Assess this cell for malaria.
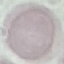
Uninfected.

preparation: thin smear
capture: smartphone camera at the microscope eyepiece
stain: Giemsa
image_type: cell patch, automatically extracted from a larger field of view and resized to 64 × 64 pixels